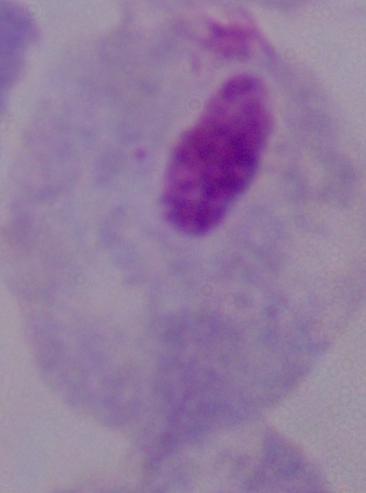

Summary:
  - Magnification: 1000x
  - Identification: trichomonad
  - Modality: photomicrograph